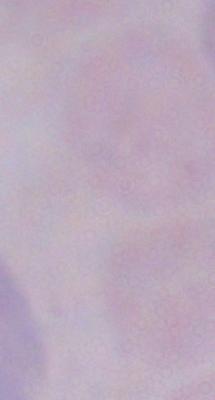

{
  "magnification": "1000x",
  "identification": "trypanosome",
  "modality": "photomicrograph"
}